Give the extent of all Trypanosoma brucei.
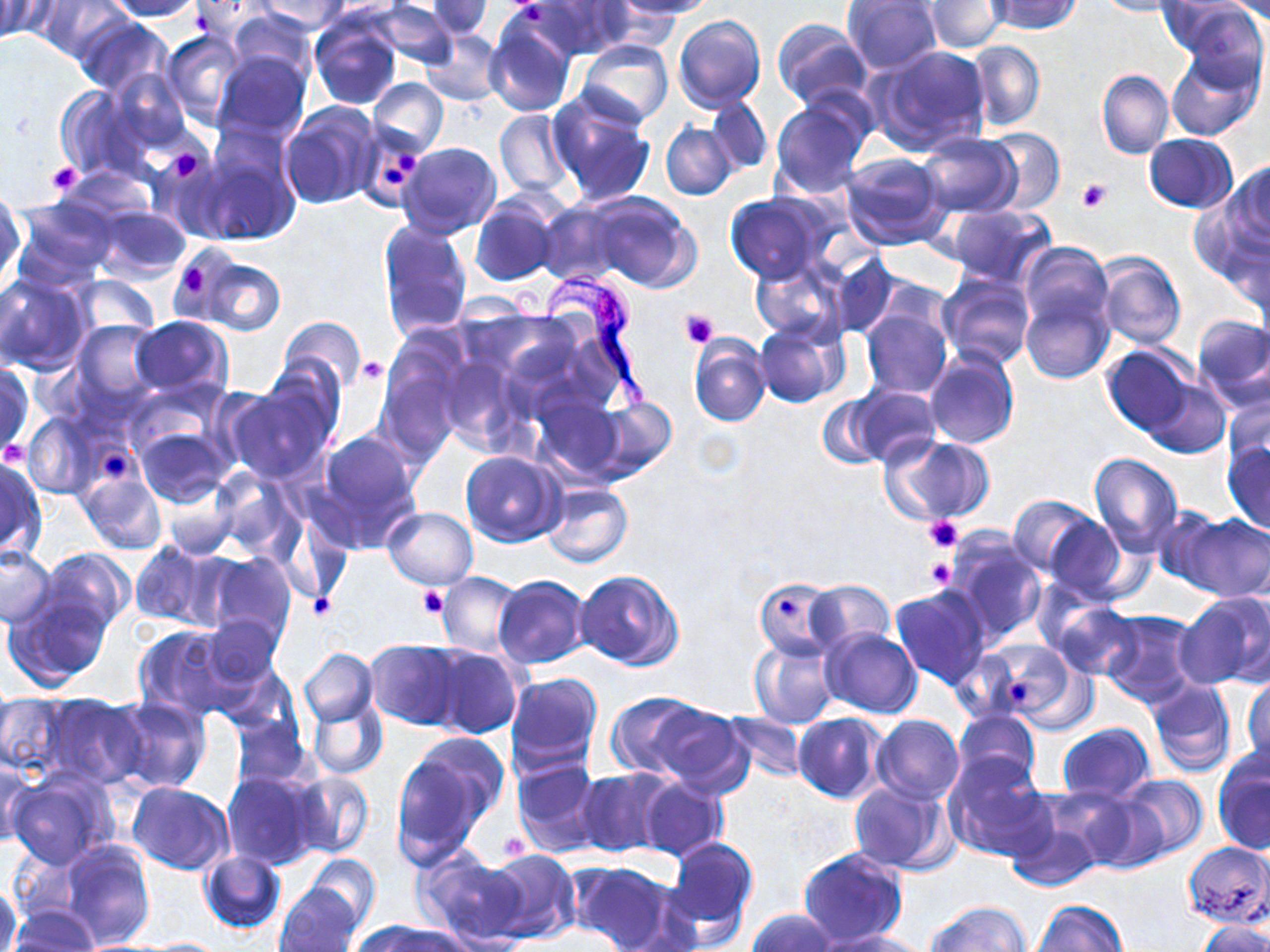

Approximate bounding boxes as (x1, y1, x2, y2) in pixels.
Trypanosoma brucei: (512, 264, 660, 411).

Platelet locations: (509, 1, 548, 21), (160, 145, 209, 185), (394, 151, 421, 173), (47, 161, 83, 197), (382, 167, 407, 187), (1076, 177, 1113, 212), (176, 261, 213, 297), (680, 309, 719, 348), (355, 357, 386, 384), (3, 441, 28, 464), (101, 448, 127, 481), (925, 516, 964, 553), (925, 557, 956, 591), (417, 585, 447, 619), (308, 595, 336, 620), (774, 596, 798, 619), (1007, 682, 1035, 708), (499, 829, 530, 862). Uninfected red blood cell locations: (38, 0, 130, 63), (102, 0, 204, 20), (188, 0, 281, 38), (253, 0, 351, 34), (372, 0, 459, 69), (534, 0, 633, 58), (612, 0, 717, 18), (986, 0, 1082, 35), (1092, 0, 1180, 17), (1157, 0, 1253, 54), (1224, 0, 1270, 23), (0, 1, 44, 41), (425, 1, 494, 39), (842, 1, 944, 76), (927, 2, 1007, 53), (1178, 3, 1267, 88), (226, 9, 317, 84), (484, 11, 577, 117), (672, 14, 765, 114), (74, 16, 173, 98), (310, 16, 401, 109), (772, 19, 871, 110), (421, 29, 504, 105), (162, 30, 247, 127), (578, 39, 673, 128), (967, 41, 1045, 131), (869, 44, 992, 156), (212, 51, 311, 144), (1166, 52, 1262, 140), (106, 67, 191, 153), (1097, 70, 1175, 160), (369, 77, 448, 156), (56, 85, 151, 182), (546, 89, 657, 205), (705, 96, 773, 174), (770, 101, 872, 197), (281, 104, 381, 208), (495, 109, 573, 197), (660, 121, 738, 199), (980, 126, 1065, 214), (197, 132, 301, 247), (918, 133, 1021, 217), (1144, 133, 1238, 213), (399, 142, 502, 238), (152, 149, 235, 242), (841, 151, 951, 250), (1229, 161, 1270, 252), (55, 169, 154, 228), (0, 192, 23, 288), (588, 193, 699, 292), (725, 194, 826, 283), (469, 196, 563, 286), (11, 198, 114, 288), (537, 201, 626, 284), (948, 204, 1055, 286), (92, 206, 190, 282), (378, 218, 472, 338), (1018, 243, 1114, 333), (1095, 252, 1187, 349), (192, 253, 289, 337), (831, 254, 899, 334), (752, 258, 846, 343), (939, 272, 1036, 370), (0, 274, 92, 376), (70, 275, 160, 339), (1021, 288, 1113, 384), (861, 305, 952, 397), (1191, 314, 1270, 411), (129, 316, 232, 401), (279, 316, 365, 397), (756, 317, 846, 407), (72, 319, 162, 409), (689, 335, 770, 425), (1102, 344, 1194, 435), (925, 349, 1018, 451), (376, 355, 467, 458), (0, 361, 33, 458), (224, 374, 338, 483), (1144, 378, 1229, 458), (848, 386, 939, 467), (1223, 394, 1270, 477), (816, 395, 885, 468), (592, 397, 677, 481), (24, 411, 103, 499), (130, 423, 234, 507), (313, 431, 423, 551), (881, 433, 993, 525), (1223, 440, 1270, 534), (461, 451, 563, 545), (1088, 452, 1183, 554), (0, 455, 45, 560), (76, 468, 167, 556), (213, 469, 304, 558), (157, 478, 240, 560), (541, 483, 633, 568), (1007, 495, 1097, 580), (383, 506, 477, 589), (1149, 508, 1231, 589), (1180, 512, 1270, 602), (1042, 515, 1127, 603), (946, 528, 1048, 647), (132, 540, 220, 631), (0, 547, 56, 628), (38, 548, 134, 638), (199, 551, 297, 650), (574, 570, 684, 671), (438, 572, 523, 657), (493, 575, 592, 669), (753, 578, 840, 660), (805, 580, 895, 654), (890, 585, 992, 691), (4, 592, 112, 691), (1174, 593, 1268, 691), (1050, 600, 1141, 680), (1100, 609, 1202, 707), (203, 614, 283, 691), (132, 622, 244, 724), (820, 628, 920, 718), (750, 639, 839, 728), (364, 640, 464, 729), (978, 640, 1087, 729), (428, 646, 523, 739), (299, 648, 377, 726), (505, 671, 603, 776), (1243, 674, 1270, 770), (1146, 678, 1236, 777), (0, 690, 74, 783), (308, 690, 387, 780), (37, 691, 148, 790), (606, 692, 709, 778), (106, 695, 211, 794), (648, 702, 752, 799), (955, 709, 1040, 791), (722, 711, 805, 782), (793, 712, 886, 802), (872, 714, 963, 804), (228, 715, 315, 794), (1057, 723, 1154, 802), (391, 738, 505, 864), (1213, 751, 1270, 856), (944, 754, 1054, 862), (512, 758, 603, 858), (0, 760, 35, 847), (7, 769, 119, 870), (574, 769, 666, 856), (222, 771, 319, 869), (286, 771, 374, 860), (1117, 774, 1208, 864), (634, 777, 728, 863), (849, 779, 955, 873), (127, 783, 233, 875), (1077, 792, 1171, 873), (1009, 803, 1106, 895), (665, 837, 759, 939), (57, 841, 154, 949), (1181, 842, 1270, 927), (481, 847, 581, 945), (796, 848, 908, 948), (198, 849, 285, 933), (412, 851, 527, 947), (304, 854, 381, 931), (568, 860, 680, 951), (0, 881, 21, 952), (276, 883, 363, 952), (1031, 898, 1126, 952), (926, 901, 1029, 952), (9, 906, 99, 951), (745, 909, 841, 952), (354, 919, 463, 952), (1195, 921, 1270, 952), (814, 929, 926, 951), (138, 938, 230, 950). Slide-level diagnosis: Trypanosoma brucei. Single field of view. May-Grünwald-Giemsa stain. Light microscopy. 1000x magnification. Thin blood film. Image is 1270×952 pixels.